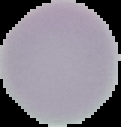
Image is 121×127 pixels. Result: negative for Plasmodium parasites. Segmented cell region on a black background. From a thin blood film.